Look for Plasmodium parasites.
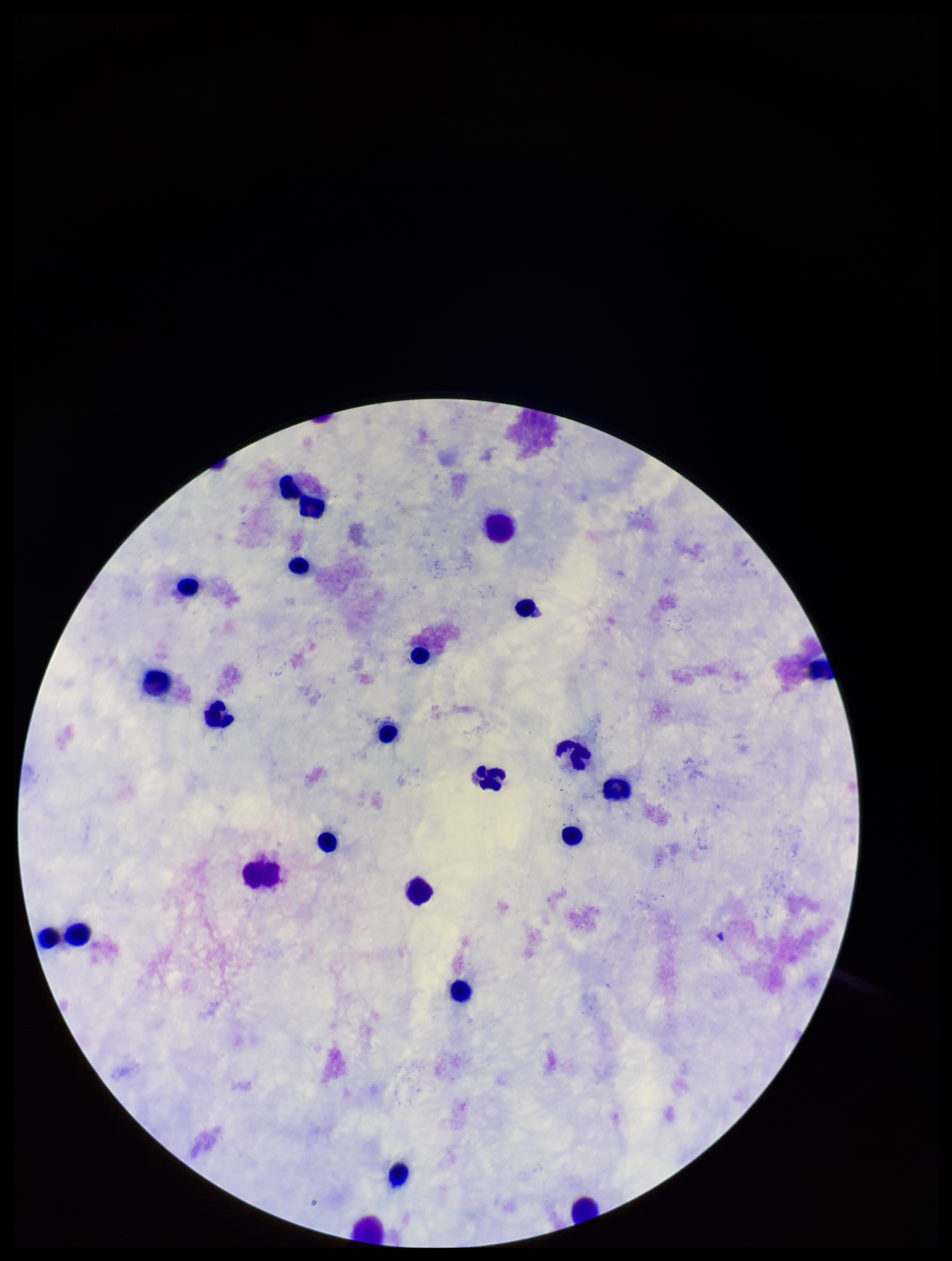
None identified.

stain = Giemsa
capture = smartphone photograph through the microscope eyepiece
parasite count = 0
leukocyte count = 22
preparation = thick smear
image size = 952×1261 pixels
field of view = one from this slide
patient malaria status = negative